Locate every blood parasite and identify its species.
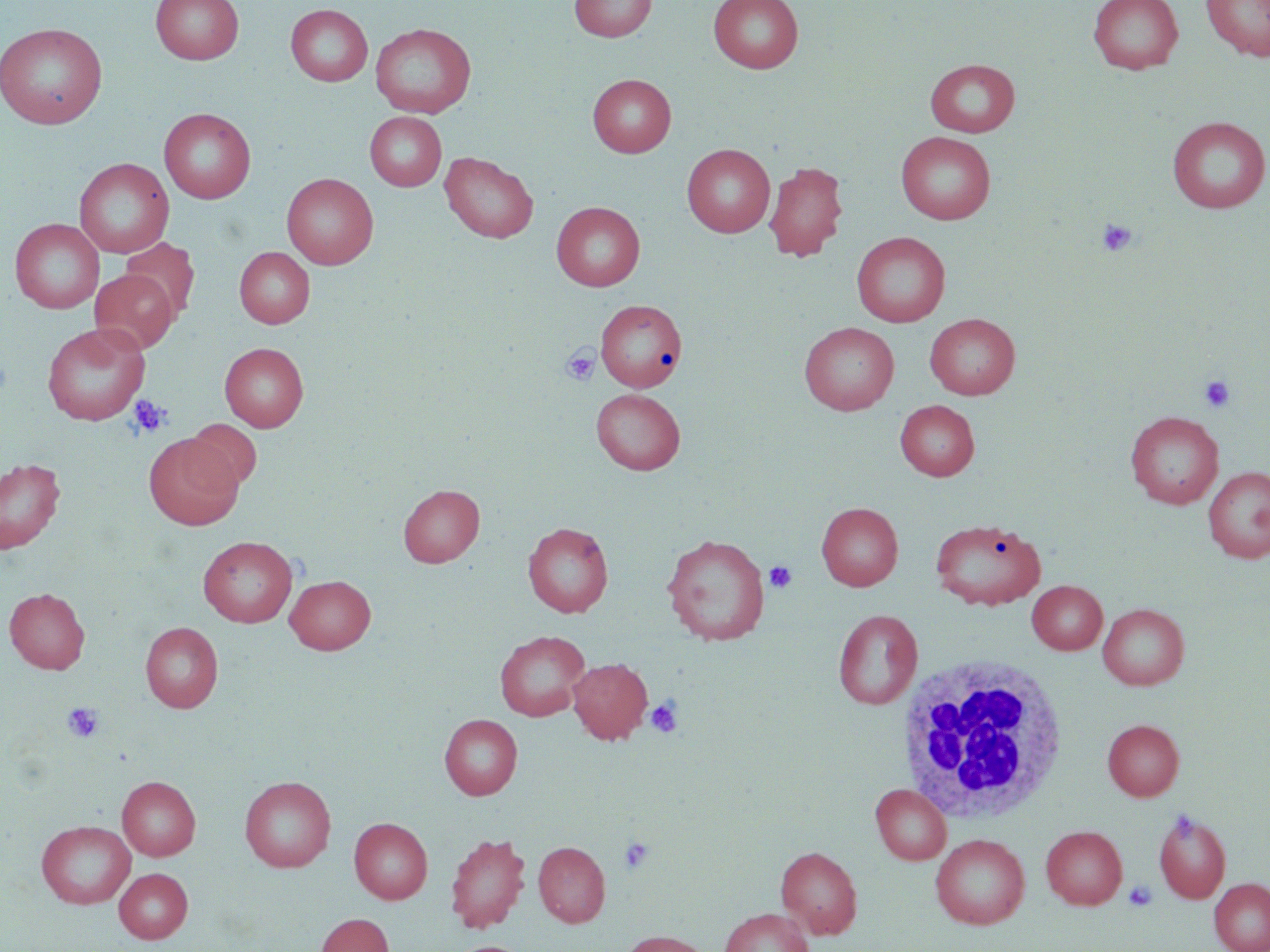

No blood parasites observed.

Approximate bounding boxes as named x1/y1/x2/y2 corners in pixels. White blood cell locations: (x1=894, y1=657, x2=1070, y2=824). Uninfected red blood cell locations: (x1=151, y1=0, x2=243, y2=65), (x1=568, y1=0, x2=657, y2=42), (x1=709, y1=0, x2=804, y2=73), (x1=1088, y1=0, x2=1184, y2=74), (x1=1201, y1=0, x2=1270, y2=61), (x1=285, y1=4, x2=373, y2=86), (x1=0, y1=22, x2=108, y2=129), (x1=370, y1=23, x2=476, y2=118), (x1=925, y1=59, x2=1020, y2=137), (x1=587, y1=73, x2=676, y2=158), (x1=159, y1=107, x2=255, y2=204), (x1=364, y1=111, x2=446, y2=191), (x1=1167, y1=115, x2=1270, y2=214), (x1=896, y1=131, x2=996, y2=224), (x1=682, y1=144, x2=775, y2=237), (x1=440, y1=152, x2=538, y2=243), (x1=74, y1=158, x2=174, y2=258), (x1=764, y1=161, x2=848, y2=262), (x1=282, y1=172, x2=378, y2=270), (x1=551, y1=201, x2=645, y2=291), (x1=10, y1=218, x2=104, y2=314), (x1=852, y1=232, x2=950, y2=327), (x1=120, y1=238, x2=200, y2=322), (x1=234, y1=247, x2=315, y2=328), (x1=90, y1=269, x2=178, y2=353), (x1=595, y1=299, x2=687, y2=392), (x1=925, y1=313, x2=1020, y2=399), (x1=799, y1=322, x2=900, y2=415), (x1=41, y1=323, x2=150, y2=425), (x1=219, y1=342, x2=308, y2=431), (x1=591, y1=388, x2=685, y2=475), (x1=895, y1=400, x2=979, y2=480), (x1=1125, y1=411, x2=1223, y2=508), (x1=184, y1=419, x2=261, y2=492), (x1=143, y1=434, x2=243, y2=530), (x1=0, y1=457, x2=66, y2=554), (x1=1202, y1=467, x2=1270, y2=563), (x1=398, y1=484, x2=484, y2=567), (x1=817, y1=502, x2=903, y2=591), (x1=929, y1=517, x2=1046, y2=610), (x1=523, y1=522, x2=613, y2=617), (x1=661, y1=533, x2=770, y2=646), (x1=198, y1=536, x2=298, y2=627), (x1=285, y1=574, x2=376, y2=654), (x1=1027, y1=580, x2=1107, y2=655), (x1=4, y1=587, x2=90, y2=674), (x1=1098, y1=603, x2=1189, y2=689), (x1=833, y1=609, x2=923, y2=709), (x1=140, y1=622, x2=223, y2=712), (x1=495, y1=630, x2=590, y2=721), (x1=567, y1=657, x2=653, y2=744), (x1=439, y1=714, x2=522, y2=800), (x1=1102, y1=719, x2=1184, y2=801), (x1=239, y1=775, x2=336, y2=872), (x1=117, y1=776, x2=200, y2=860), (x1=870, y1=784, x2=951, y2=864), (x1=1153, y1=809, x2=1231, y2=903), (x1=349, y1=817, x2=433, y2=904), (x1=36, y1=819, x2=136, y2=909), (x1=1041, y1=825, x2=1127, y2=909), (x1=445, y1=831, x2=530, y2=933), (x1=930, y1=833, x2=1030, y2=929), (x1=534, y1=841, x2=610, y2=927), (x1=775, y1=845, x2=862, y2=938), (x1=114, y1=868, x2=193, y2=944), (x1=1209, y1=877, x2=1270, y2=952), (x1=719, y1=908, x2=813, y2=952), (x1=315, y1=913, x2=394, y2=952), (x1=618, y1=929, x2=715, y2=952). Platelet locations: (x1=1097, y1=217, x2=1139, y2=258), (x1=561, y1=346, x2=599, y2=386), (x1=1199, y1=375, x2=1237, y2=413), (x1=127, y1=394, x2=171, y2=439), (x1=764, y1=561, x2=797, y2=593), (x1=646, y1=697, x2=684, y2=738), (x1=62, y1=702, x2=103, y2=742), (x1=618, y1=837, x2=655, y2=873), (x1=1123, y1=880, x2=1158, y2=911). Slide-level diagnosis: no evidence of blood parasites. Optical microscopy. May-Grünwald-Giemsa stain. Thin blood film. Image is 1270×952 pixels. 1000x magnification. One field of a larger specimen.